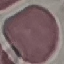
Summary:
  - Malaria status: uninfected
  - Image type: cell patch, automatically extracted from a larger field of view and resized to 64 × 64 pixels
  - Stain: Giemsa
  - Preparation: thin blood smear
  - Capture: smartphone through the microscope eyepiece